Outline each blood parasite and name the species.
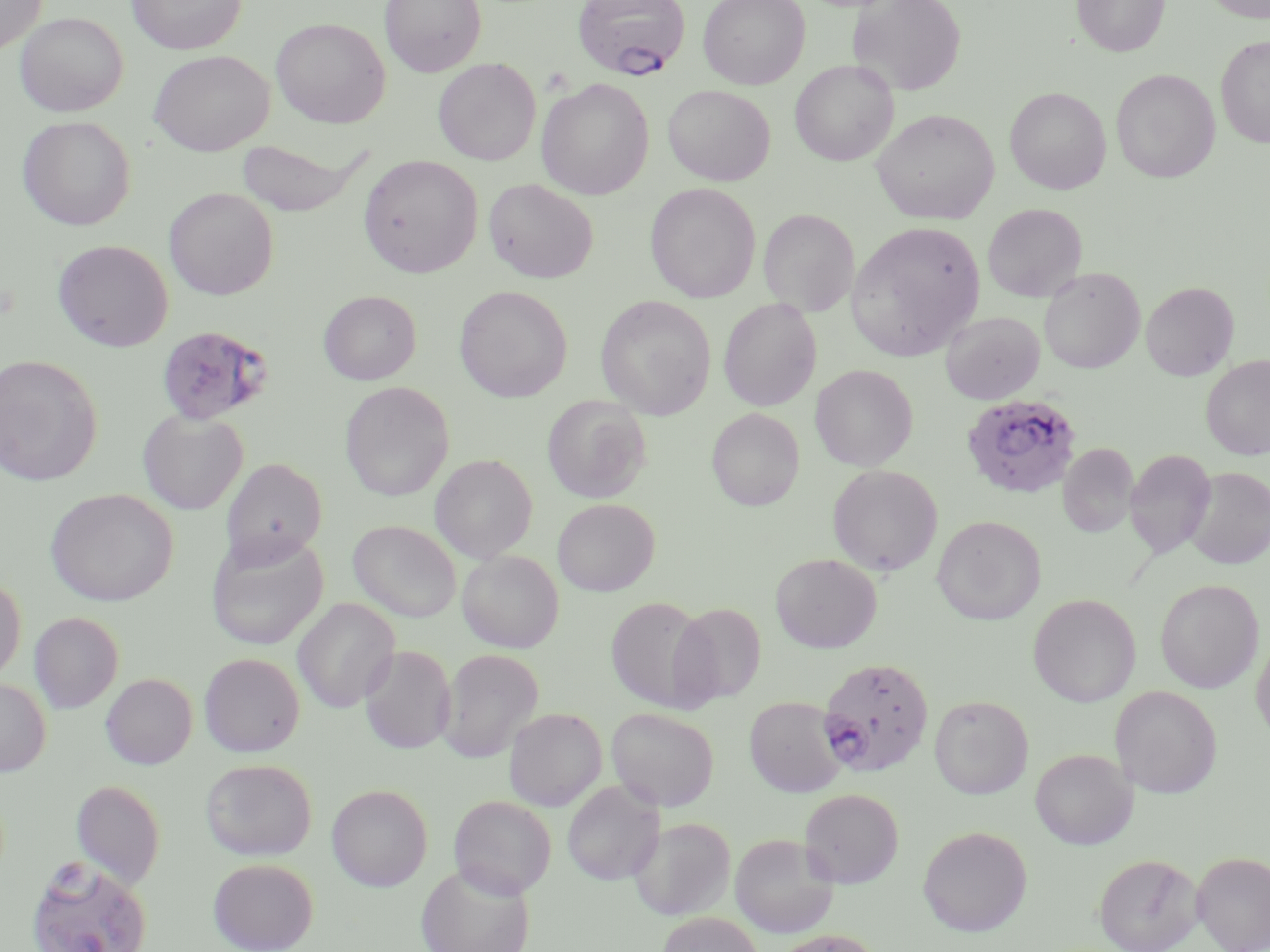

Approximate bounding boxes as (x1, y1, x2, y2) in pixels.
Plasmodium falciparum-infected red blood cells: (572, 0, 691, 81), (156, 324, 275, 426), (960, 392, 1082, 499), (817, 656, 939, 777), (25, 856, 154, 952).
No Plasmodium ovale, Plasmodium malariae, Plasmodium vivax, Babesia divergens, or Trypanosoma brucei observed.

Summary:
  - Uninfected red blood cell locations: (0, 0, 48, 55), (127, 0, 245, 54), (379, 0, 486, 76), (698, 0, 810, 90), (848, 0, 966, 96), (1072, 0, 1170, 57), (1202, 0, 1270, 22), (15, 11, 128, 116), (271, 17, 391, 128), (1215, 35, 1270, 148), (149, 50, 274, 156), (433, 58, 541, 165), (790, 59, 899, 165), (1111, 69, 1220, 183), (536, 78, 654, 200), (663, 85, 775, 185), (1005, 87, 1111, 194), (871, 108, 999, 225), (17, 116, 136, 230), (234, 138, 366, 217), (358, 155, 483, 278), (483, 178, 599, 283), (644, 183, 760, 302), (163, 187, 279, 300), (982, 203, 1087, 302), (758, 209, 860, 317), (846, 221, 986, 361), (52, 239, 174, 352), (1038, 267, 1144, 374), (1140, 281, 1239, 381), (454, 285, 573, 402), (318, 290, 421, 385), (594, 295, 716, 420), (718, 297, 822, 411), (940, 311, 1045, 404), (0, 354, 103, 486), (1201, 354, 1270, 460), (811, 364, 917, 471), (820, 365, 924, 576), (340, 381, 455, 501), (542, 394, 652, 502), (706, 408, 805, 511), (137, 410, 248, 515), (1058, 443, 1138, 538), (1125, 449, 1216, 559), (430, 454, 538, 562), (221, 457, 327, 566), (828, 464, 943, 576), (1185, 467, 1270, 569), (45, 488, 179, 607), (552, 498, 660, 596), (932, 515, 1046, 625), (349, 520, 461, 623), (206, 532, 328, 651), (457, 549, 564, 653), (771, 553, 881, 653), (0, 574, 26, 686), (1155, 579, 1264, 693), (1028, 594, 1141, 707), (606, 596, 714, 711), (292, 598, 400, 713), (670, 602, 767, 706), (29, 612, 123, 714), (1251, 633, 1270, 744), (359, 644, 456, 754), (438, 648, 544, 762), (199, 652, 304, 757), (100, 673, 197, 770), (0, 678, 51, 776), (1110, 686, 1222, 798), (929, 695, 1034, 799), (744, 696, 847, 797), (504, 707, 607, 811), (606, 707, 720, 811), (1030, 748, 1137, 850), (200, 758, 317, 861), (70, 780, 166, 888), (562, 780, 664, 885), (326, 784, 433, 891), (799, 788, 904, 888), (449, 795, 557, 898), (631, 817, 736, 921), (917, 825, 1033, 937), (729, 833, 840, 938), (1192, 851, 1270, 951), (1093, 852, 1204, 952), (208, 857, 318, 952), (416, 862, 535, 952), (657, 913, 764, 951), (769, 929, 885, 952)
  - Slide-level diagnosis: Plasmodium falciparum
  - Stain: May-Grünwald-Giemsa
  - Magnification: 1000x
  - Modality: optical microscopy
  - Field of view: one of a larger specimen
  - Preparation: thin blood smear
  - Image size: 1270×952 pixels